Point out each leukocyte.
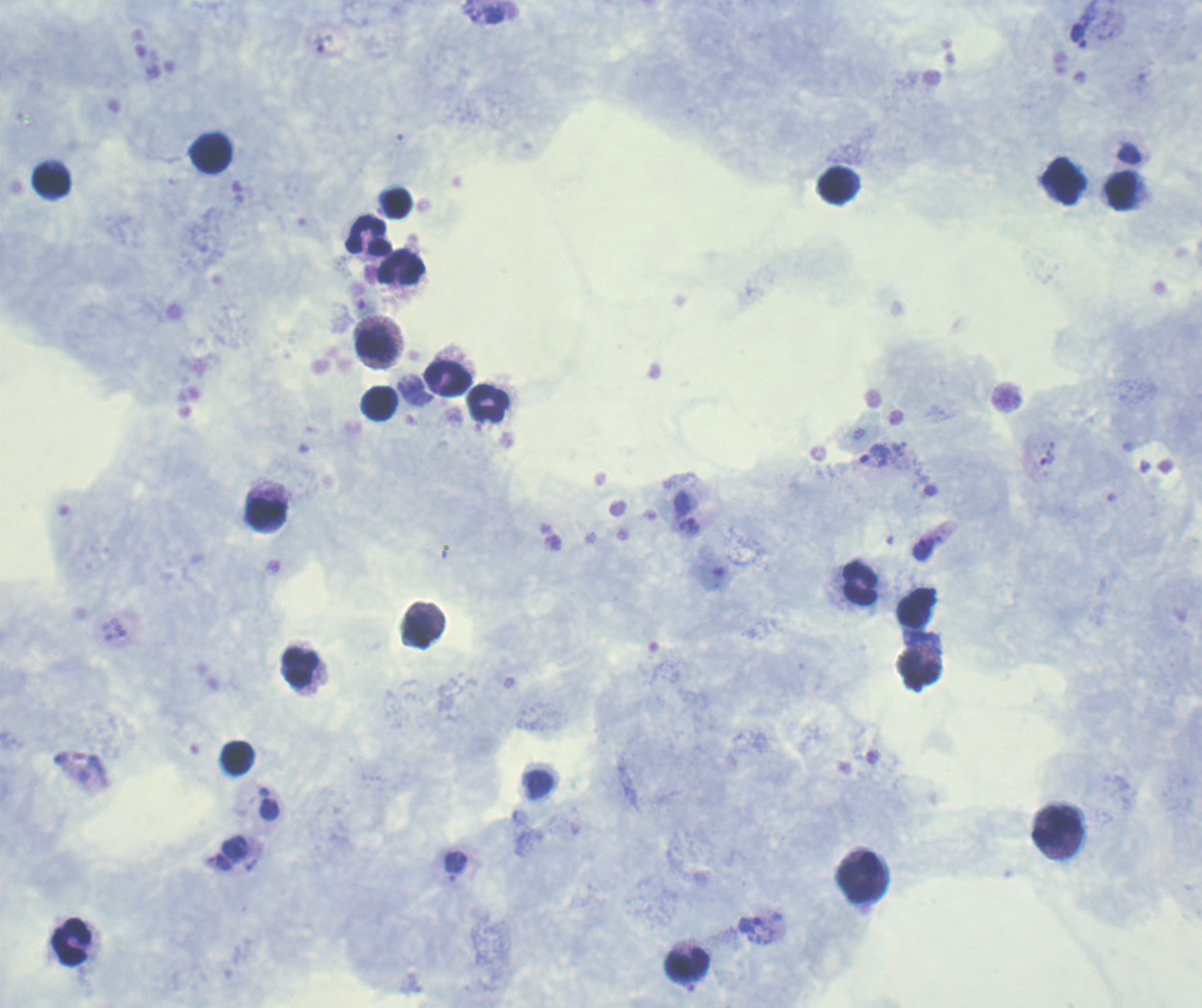
Approximate object centers, in pixels from the top-left corner.
Leukocytes: (x=212, y=153), (x=52, y=180), (x=1066, y=180), (x=838, y=185), (x=1122, y=191), (x=398, y=203), (x=369, y=236), (x=401, y=267), (x=376, y=343), (x=448, y=379), (x=488, y=402), (x=379, y=403), (x=266, y=513), (x=860, y=583), (x=917, y=609), (x=301, y=668), (x=920, y=668), (x=238, y=758), (x=1057, y=828), (x=858, y=877), (x=72, y=942), (x=688, y=963).

coordinate format = approximate object centers, in pixels from the top-left corner
trophozoite locations = (x=1079, y=37), (x=321, y=43), (x=874, y=455), (x=1048, y=458), (x=923, y=549), (x=270, y=808), (x=456, y=862), (x=751, y=925)
context = previously used in a real diagnosis
magnification = 100x
background quality = good
stain = Romanowsky
result = malaria parasites detected
image size = 1202×1008 pixels
field of view = single
preparation = thick blood smear
coloration quality = good